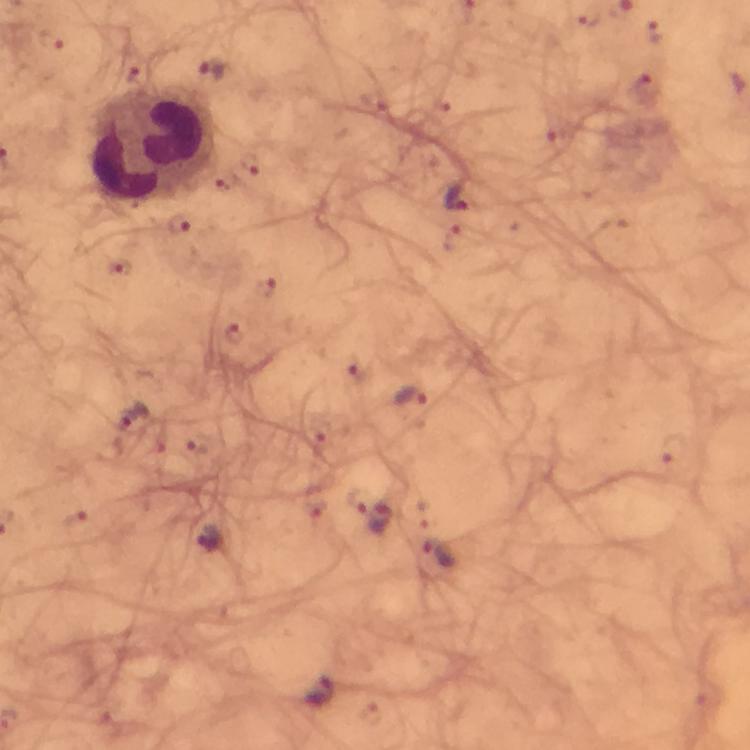
capture = smartphone camera through the microscope
context = from a diagnostic examination for malaria
immersion oil = applied
stain = Giemsa
cropped from = one field of view
leukocyte locations = approximate centers as [x, y] in pixels: [150, 145]
malaria parasite locations = approximate centers as [x, y] in pixels: [456, 196], [179, 224], [234, 336], [359, 370], [413, 398], [133, 417], [374, 514], [211, 539], [440, 557], [320, 694]
image size = 750×750 pixels
preparation = thick smear
magnification = 100x